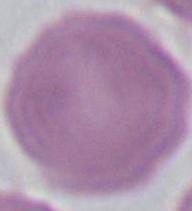
identification = erythrocyte
magnification = 1000x
modality = micrograph